Find the red blood cells and label each as Plasmodium falciparum-infected, uninfected, or of indeterminate infection status.
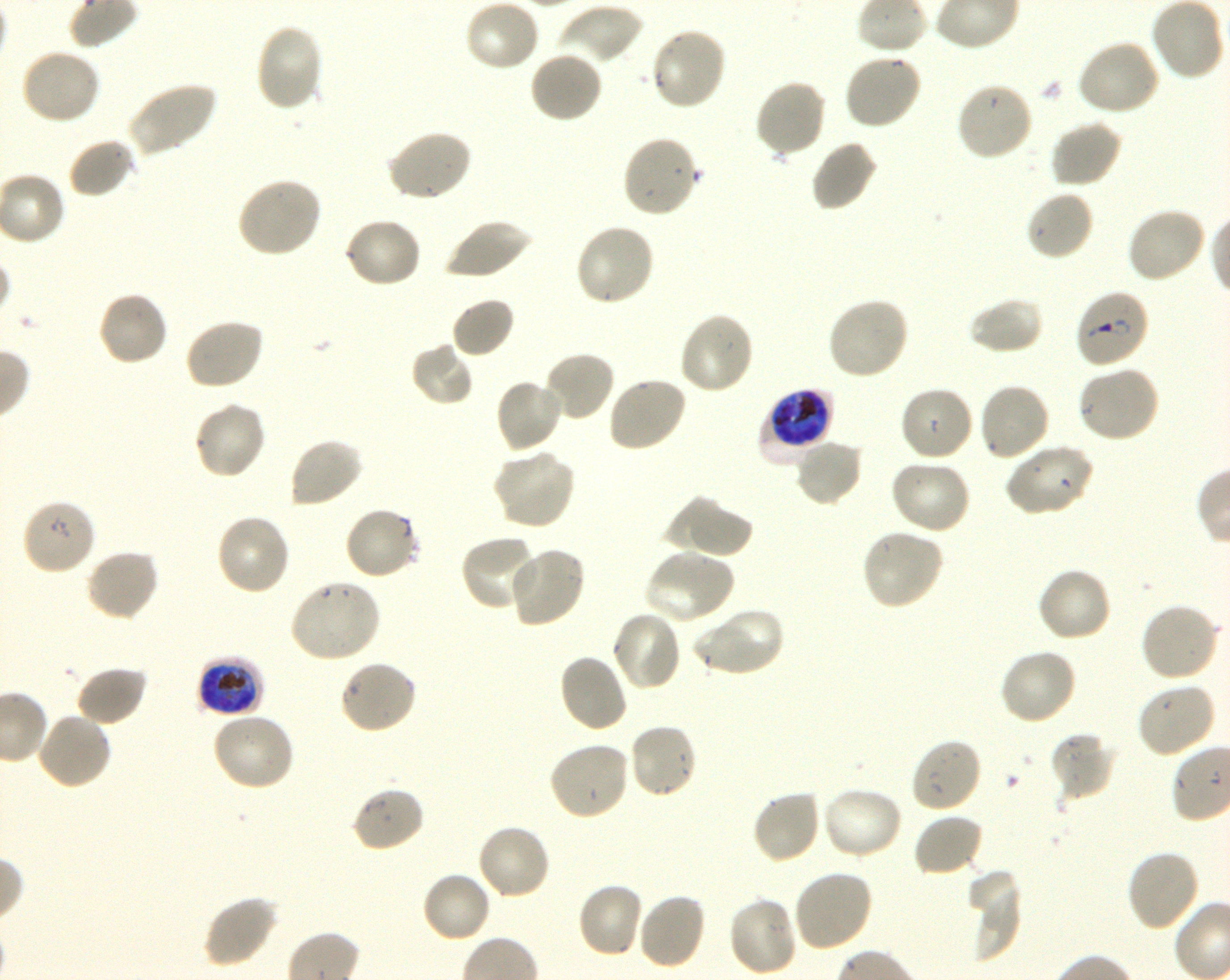

Approximate bounding boxes as [x1, y1, x2, y2] in pixels. Not every red blood cell is marked. A life-cycle stage — or a range of stages, where the recorded stages span more than one — follows each staged infected red blood cell.
Infected red blood cells: [1074, 288, 1150, 370] ring; [758, 389, 833, 465] late trophozoite to early schizont; [196, 656, 264, 717] late trophozoite to early schizont.
Uninfected red blood cells: [464, 0, 541, 72], [557, 3, 644, 67], [253, 22, 326, 112], [649, 26, 728, 112], [1076, 39, 1163, 117], [19, 47, 102, 125], [528, 50, 603, 123], [842, 53, 923, 131], [754, 79, 827, 161], [125, 81, 217, 157], [954, 81, 1034, 162], [1049, 118, 1123, 188], [385, 129, 473, 203], [621, 135, 700, 220], [67, 137, 136, 199], [809, 140, 878, 214], [234, 178, 322, 259], [1024, 190, 1095, 262], [1126, 206, 1207, 284], [344, 216, 424, 288], [442, 218, 533, 281], [573, 222, 655, 308], [96, 290, 170, 368], [450, 296, 516, 359], [826, 296, 910, 381], [968, 297, 1044, 355], [677, 311, 756, 396], [184, 317, 265, 391], [409, 342, 476, 407], [542, 350, 615, 422], [1075, 366, 1162, 444], [606, 376, 688, 453], [494, 377, 564, 455], [977, 382, 1051, 463], [898, 385, 974, 463], [192, 400, 267, 481], [287, 437, 364, 510], [793, 438, 864, 508], [1003, 443, 1093, 517], [490, 449, 576, 531], [889, 458, 972, 534], [667, 497, 752, 558], [20, 498, 97, 576], [343, 506, 421, 581], [214, 512, 291, 596], [860, 527, 945, 612], [459, 534, 539, 614], [507, 546, 586, 629], [84, 548, 160, 622], [643, 549, 735, 625], [1035, 566, 1113, 643], [288, 579, 382, 664], [1139, 601, 1221, 682], [691, 606, 784, 678], [611, 610, 682, 692], [997, 648, 1078, 727], [557, 653, 629, 733], [337, 659, 417, 735], [75, 665, 147, 727], [1135, 682, 1217, 759], [211, 710, 296, 791], [35, 711, 113, 790], [627, 722, 699, 800], [1050, 731, 1116, 803], [910, 736, 983, 813], [547, 739, 631, 821], [350, 785, 426, 853], [821, 786, 904, 861], [750, 789, 822, 866], [912, 812, 984, 878], [476, 823, 552, 901], [1125, 848, 1200, 933], [792, 869, 873, 952], [421, 870, 493, 943], [968, 870, 1023, 963], [577, 882, 644, 960], [636, 892, 707, 970], [201, 895, 279, 968], [726, 895, 799, 978].
No red blood cells of indeterminate infection status observed.

Thin blood smear. 100x oil-immersion objective, numerical aperture 1.30. Giemsa stain. Blood group of the donor: O+. Image is 1230×980 pixels. Shaking in-vitro culture of Plasmodium falciparum strain 3D7. One field from this slide.